Locate every blood parasite and identify its species.
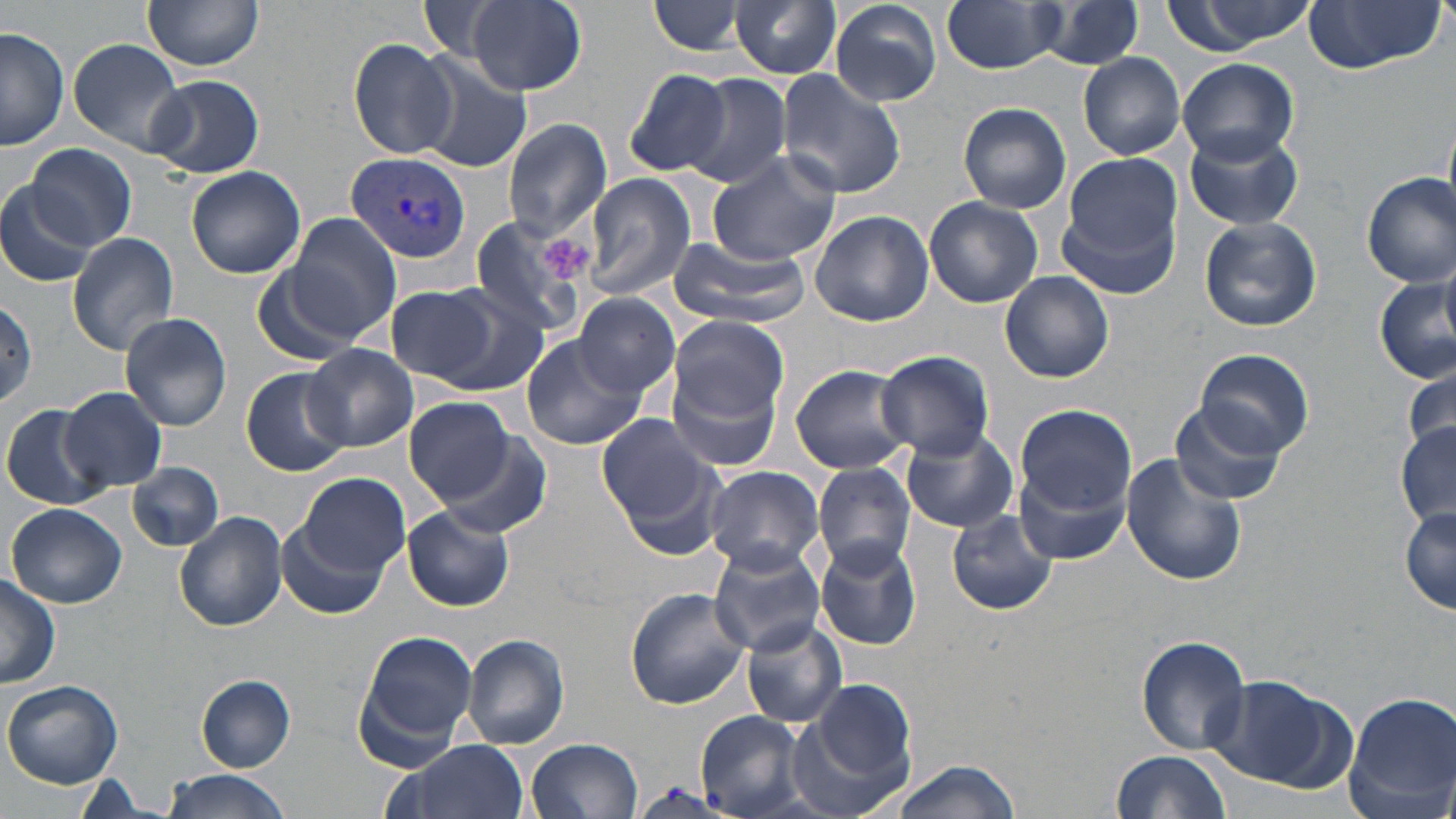
Approximate bounding boxes as (x1,y1)-(x2,y2) corner pairs in pixels.
Plasmodium vivax-infected red blood cells: (347,152)-(471,263).
No Plasmodium falciparum, Plasmodium ovale, Plasmodium malariae, Babesia divergens, or Trypanosoma brucei observed.

slide-level diagnosis = Plasmodium vivax
magnification = 1000x
image size = 1456×819 pixels
stain = May-Grünwald-Giemsa
modality = light microscopy
field of view = single
preparation = thin blood smear
uninfected red blood cell locations = approximate bounding boxes as (x1,y1)-(x2,y2) corner pairs in pixels: (143,0)-(265,72), (467,0)-(587,93), (827,0)-(943,107), (1160,0)-(1319,57), (650,1)-(749,57), (731,1)-(842,79), (943,1)-(1065,74), (1037,1)-(1146,74), (1300,1)-(1448,75), (420,2)-(508,62), (1,27)-(68,152), (349,37)-(460,161), (67,38)-(188,153), (411,50)-(533,172), (1079,52)-(1186,161), (1174,58)-(1300,165), (623,68)-(733,177), (776,70)-(907,200), (684,73)-(792,189), (146,75)-(264,178), (958,102)-(1071,213), (501,118)-(613,241), (1183,125)-(1304,232), (25,142)-(138,249), (707,150)-(843,268), (1065,153)-(1183,260), (186,166)-(307,279), (583,173)-(696,301), (1361,173)-(1456,287), (0,182)-(96,288), (923,196)-(1044,308), (1058,198)-(1179,300), (808,209)-(935,327), (284,212)-(402,344), (1199,215)-(1324,330), (465,216)-(595,343), (67,232)-(180,355), (667,235)-(810,328), (1439,256)-(1456,356), (250,265)-(353,366), (999,271)-(1114,383), (1375,272)-(1455,384), (388,286)-(497,383), (423,288)-(559,399), (573,292)-(681,398), (0,294)-(39,407), (118,312)-(232,432), (670,316)-(789,421), (522,336)-(643,450), (304,343)-(418,452), (1195,348)-(1312,459), (876,350)-(995,459), (789,363)-(915,475), (666,364)-(784,475), (1403,366)-(1456,454), (240,368)-(352,476), (61,387)-(167,492), (405,397)-(519,503), (1170,399)-(1286,507), (1,402)-(111,511), (1014,405)-(1135,519), (596,413)-(712,524), (1395,424)-(1456,527), (901,429)-(1019,532), (441,436)-(551,541), (1120,454)-(1248,586), (1015,461)-(1131,566), (128,462)-(223,551), (812,462)-(915,575), (702,465)-(825,571), (300,475)-(409,578), (6,503)-(128,608), (403,507)-(514,612), (946,507)-(1059,617), (1400,507)-(1456,613), (173,511)-(286,630), (276,515)-(391,620), (815,538)-(921,650), (708,542)-(828,655), (0,572)-(61,690), (625,588)-(750,709), (742,619)-(848,728), (359,630)-(477,750), (461,633)-(570,750), (1135,635)-(1251,754), (1203,674)-(1346,790), (196,675)-(296,771), (800,679)-(916,805), (3,680)-(124,789), (1344,692)-(1456,818), (695,710)-(809,816), (527,738)-(643,819), (394,739)-(528,819), (1110,751)-(1233,819), (893,757)-(1021,819), (159,770)-(295,819), (69,773)-(157,816)